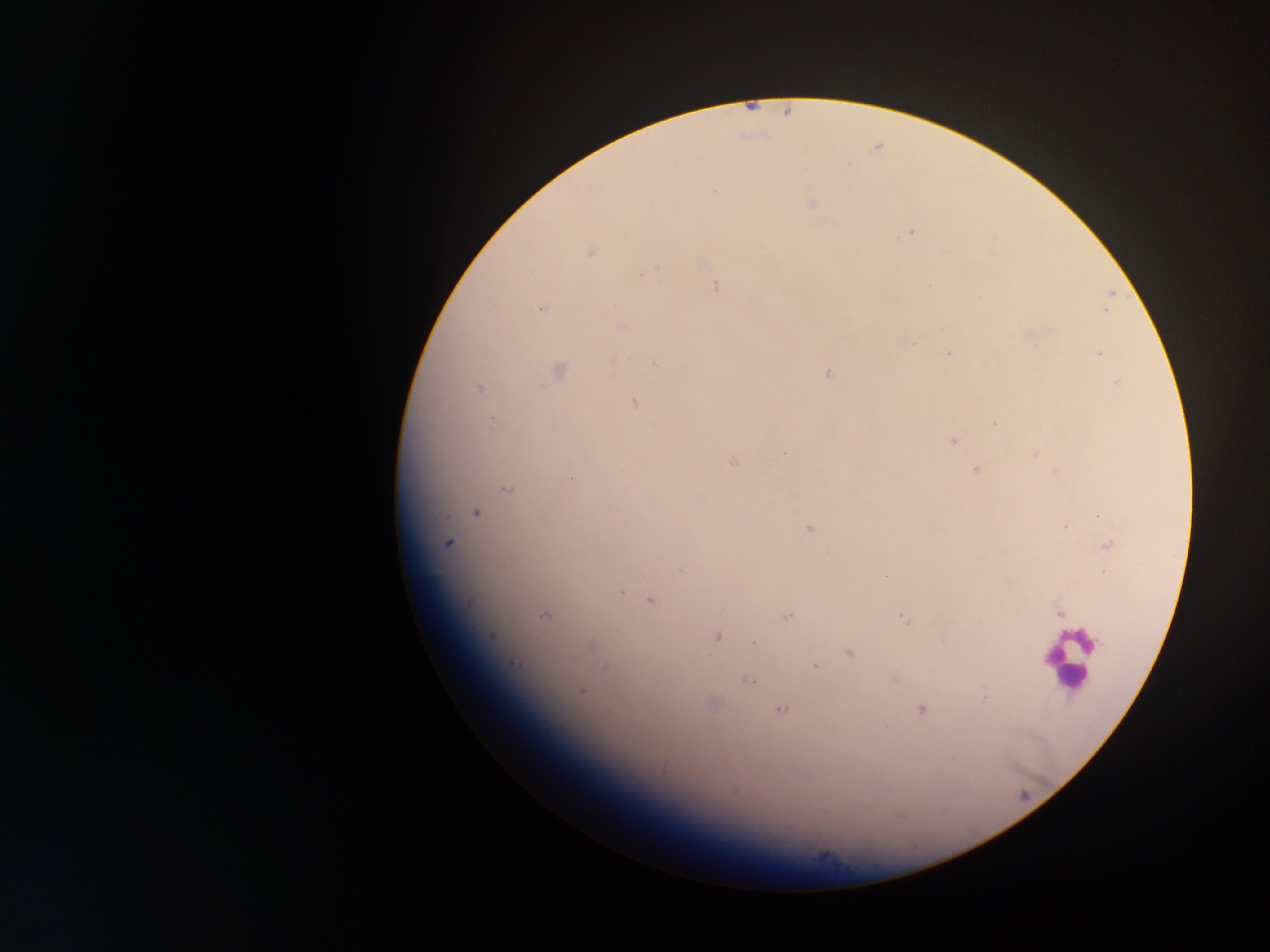

malaria parasite locations = approximate centers as x y in pixels: 911 232; 592 251; 658 265; 640 276; 716 287; 979 296; 542 309; 1107 309; 620 327; 1048 328; 909 341; 1100 353; 947 354; 612 358; 655 363; 828 372; 1116 382; 480 388; 633 402; 494 421; 994 424; 951 440; 1033 452; 783 453; 732 463; 974 470; 1053 472; 573 480; 506 488; 475 512; 1099 516; 1066 526; 808 529; 1106 543; 449 545; 680 570; 1103 573; 649 600; 1058 613; 788 615; 899 615; 495 635; 718 638; 753 643; 849 654; 513 662; 814 664; 749 681; 582 690; 983 699; 921 709; 782 710; 663 769
country = Ghana
preparation = thick blood film
capture = mobile-phone photograph through a microscope
image size = 1270×952 pixels
field of view = single